Describe the morphology of the erythrocytes.
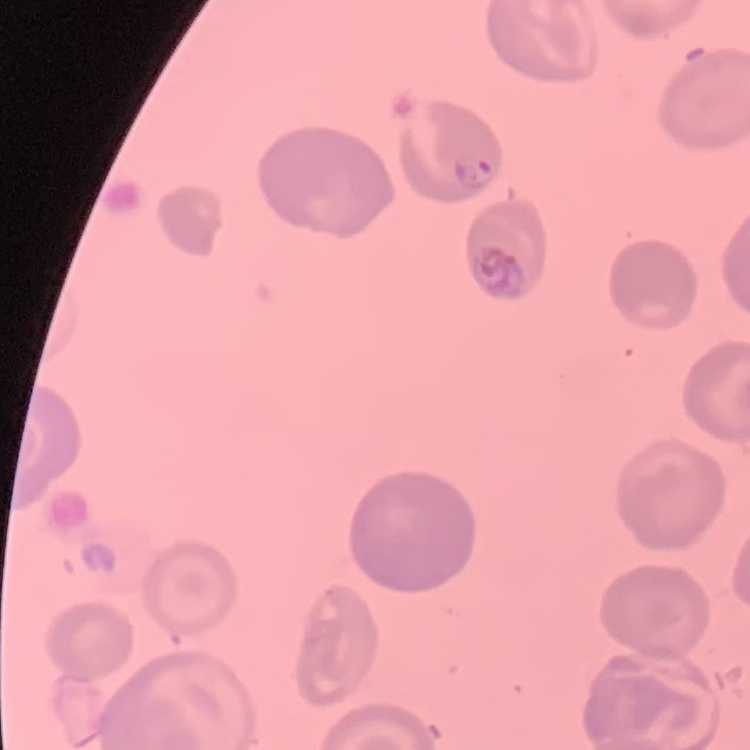
No rouleaux formation.

One tile cut from a larger photomicrograph. Thin peripheral smear. Field's or Giemsa stain.